Point out each Plasmodium parasite and each leukocyte.
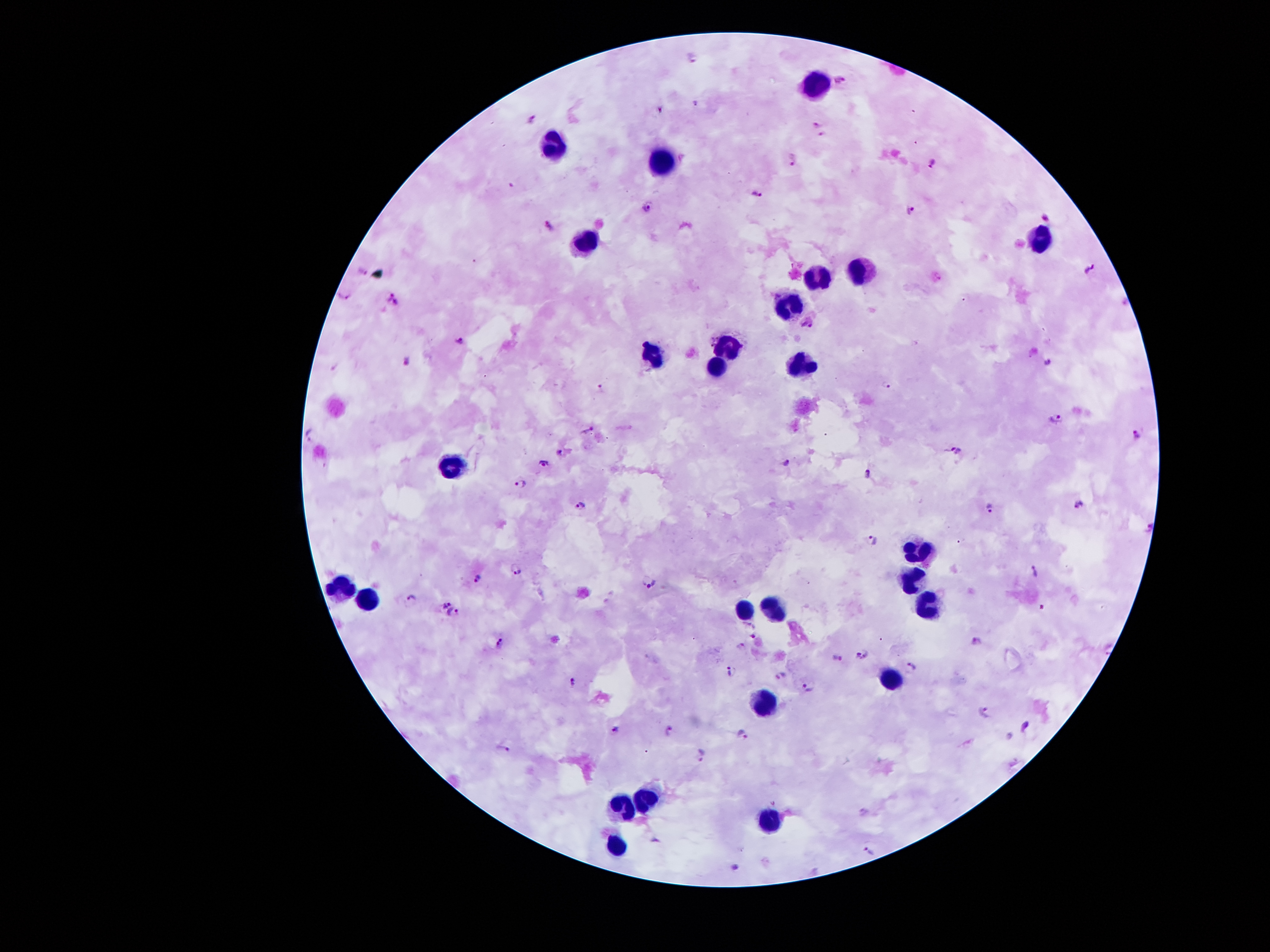
Approximate centers as [x, y] in pixels.
Plasmodium parasites: [693, 56], [841, 78], [660, 110], [531, 118], [815, 122], [820, 135], [934, 161], [793, 163], [757, 197], [646, 207], [910, 209], [1045, 216], [550, 225], [363, 268], [1088, 268], [346, 297], [392, 300], [806, 323], [459, 337], [712, 340], [405, 360], [1050, 363], [886, 384], [601, 389], [1053, 417], [589, 430], [310, 435], [1136, 435], [957, 450], [561, 451], [543, 463], [787, 463], [868, 474], [520, 485], [581, 502], [1079, 505], [991, 506], [1148, 526], [874, 537], [515, 568], [1034, 568], [478, 577], [653, 582], [411, 598], [445, 602], [1042, 608], [455, 612], [754, 630], [976, 638], [499, 639], [741, 646], [860, 656], [836, 657], [914, 667], [730, 670], [781, 674], [571, 680], [807, 686], [986, 712], [1025, 725], [614, 728], [669, 728], [744, 731], [504, 747], [700, 754], [864, 812], [655, 840], [870, 849], [733, 866].
Leukocytes: [811, 85], [551, 146], [664, 160], [1039, 239], [585, 241], [858, 267], [813, 277], [789, 306], [726, 347], [649, 356], [804, 364], [715, 370], [453, 462], [921, 552], [910, 582], [340, 591], [368, 599], [929, 607], [744, 609], [774, 611], [888, 680], [762, 700], [640, 796], [619, 805], [769, 816], [615, 842].

Summary:
  - Image size: 1270×952 pixels
  - Capture: smartphone through the microscope eyepiece
  - Field of view: single
  - Stain: Giemsa
  - Preparation: thick peripheral-blood smear
  - Magnification: 100x
  - Patient malaria status: infected with Plasmodium falciparum